Name the parasite shown.
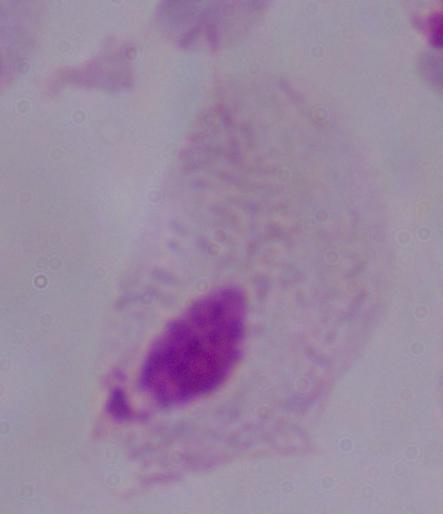
A trichomonad.

{
  "magnification": "1000x",
  "modality": "photomicrograph"
}